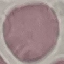
Summary:
  - Malaria status: uninfected
  - Preparation: thin blood smear
  - Stain: Giemsa
  - Image type: automatically extracted cell patch, resized to 64 × 64 pixels
  - Capture: smartphone camera at the microscope eyepiece